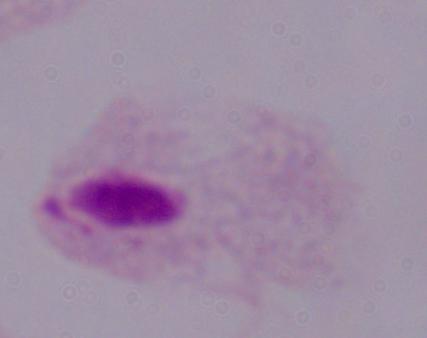 Captured at 1000x magnification. Micrograph. A trichomonad is seen.